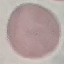

Summary:
  - Malaria status: uninfected
  - Stain: Giemsa
  - Capture: smartphone through the microscope eyepiece
  - Image type: cell patch, automatically extracted from a larger field of view and resized to 64 × 64 pixels
  - Preparation: thin blood smear